Name the cell type shown.
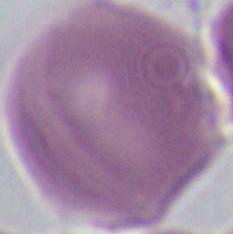
This is an erythrocyte.

Summary:
  - Modality: micrograph
  - Magnification: 1000x